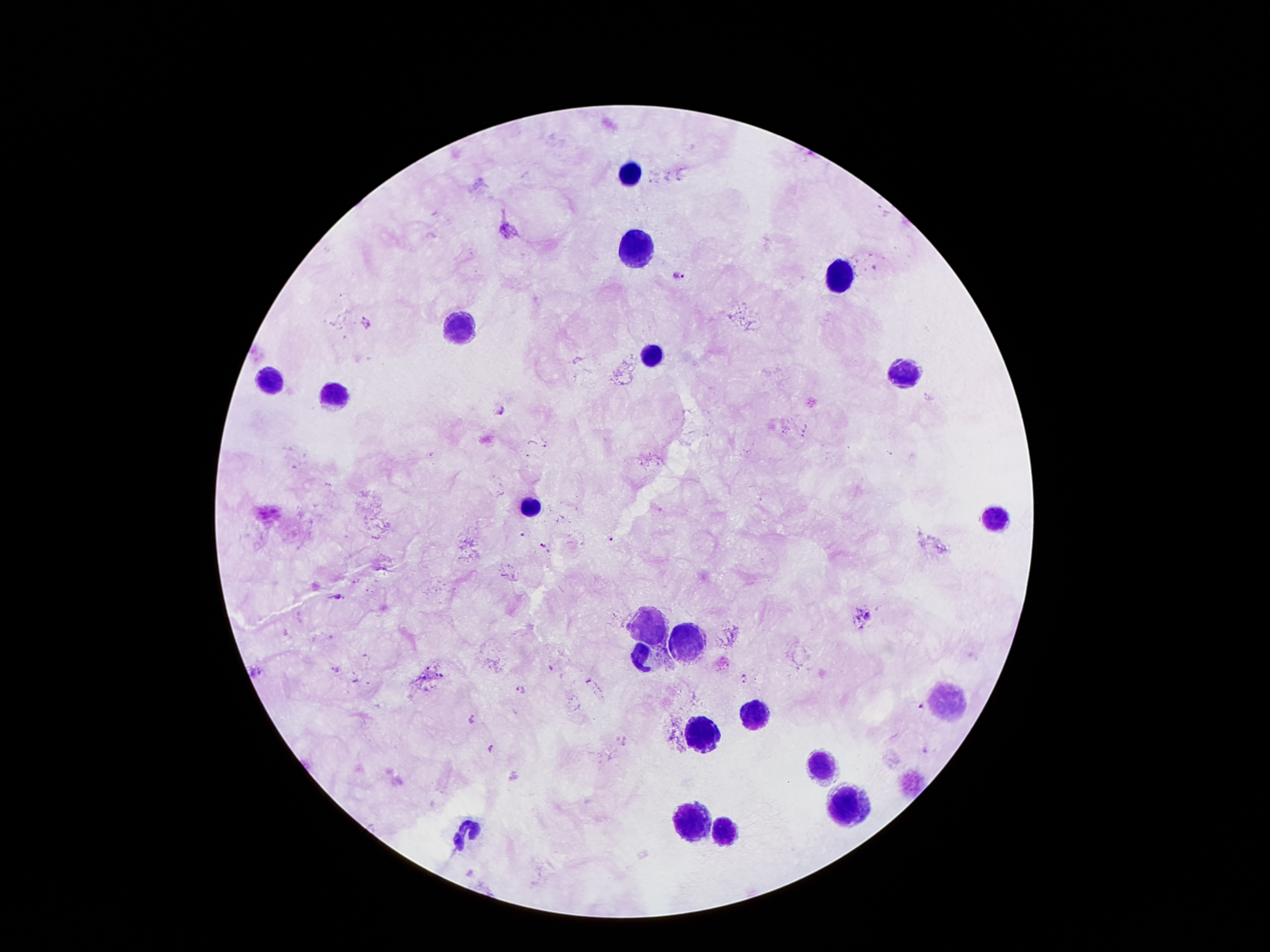
Approximate centers as {x, y} in pixels.
Summary:
  - Malaria parasite locations: {679, 275}, {365, 323}, {498, 409}, {610, 539}, {542, 545}, {338, 596}, {744, 679}, {519, 690}, {921, 708}, {472, 719}, {490, 748}
  - Leukocyte locations: {634, 170}, {634, 249}, {836, 275}, {461, 327}, {652, 356}, {902, 374}, {270, 379}, {336, 396}, {528, 504}, {996, 519}, {650, 621}, {688, 643}, {645, 657}, {945, 700}, {757, 713}, {705, 733}, {826, 764}, {841, 806}, {695, 819}, {721, 829}, {469, 832}
  - Field of view: single
  - Patient malaria status: infected with Plasmodium falciparum
  - Stain: Giemsa
  - Capture: smartphone through the microscope eyepiece
  - Image size: 1270×952 pixels
  - Magnification: 100x
  - Preparation: thick blood film